Name the parasite shown.
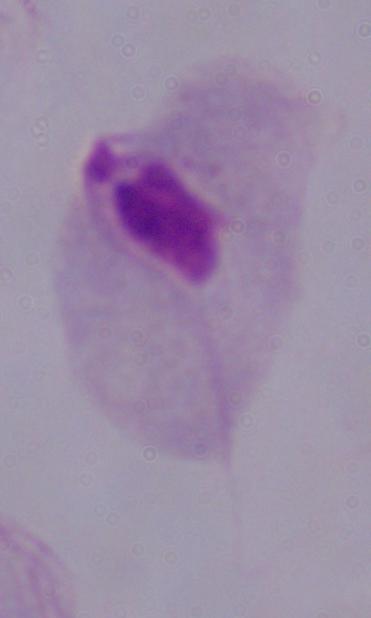
A trichomonad.

Summary:
  - Magnification: 1000x
  - Modality: photomicrograph